Look for parasitized red blood cells.
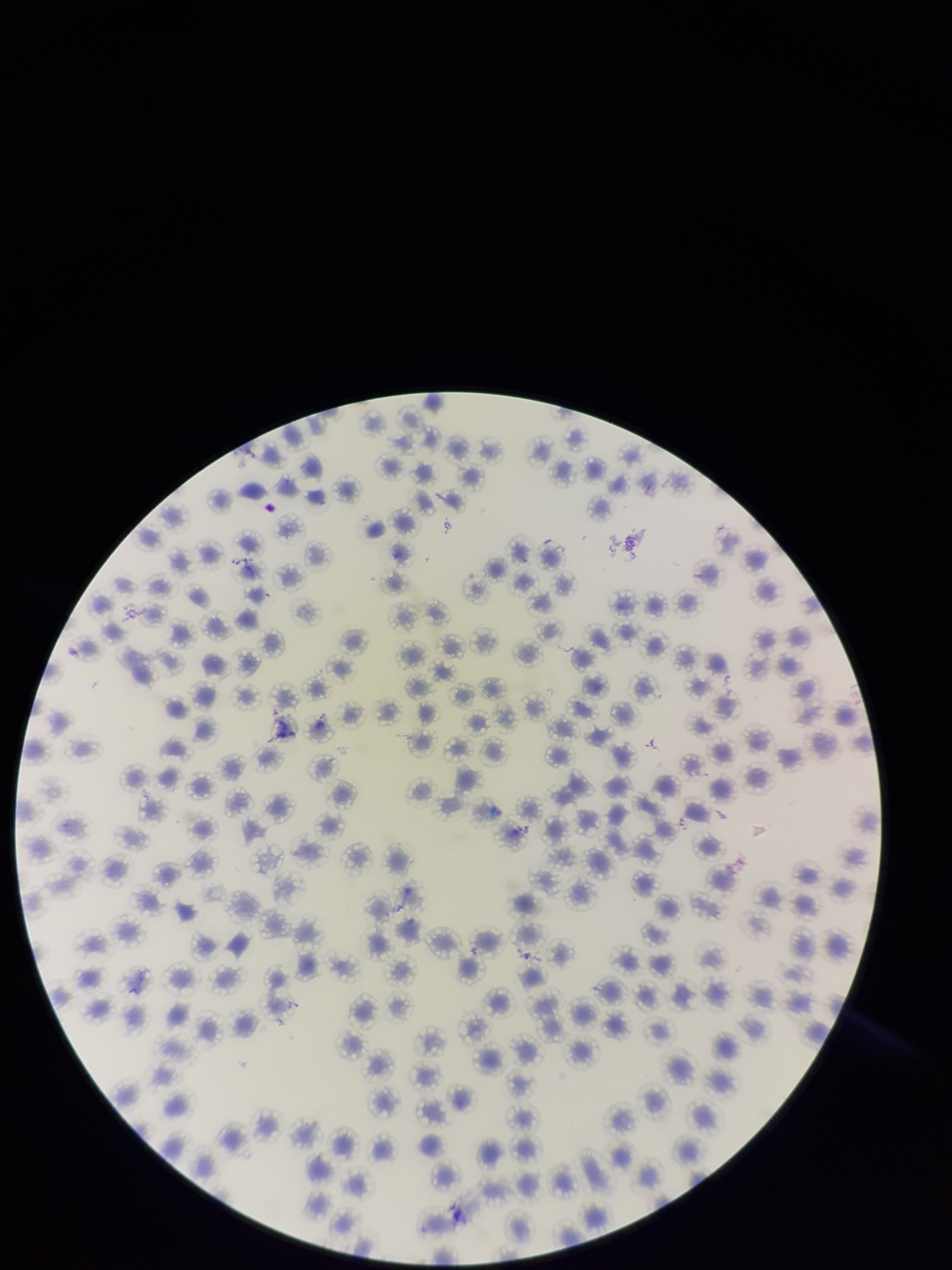
None seen.

Parasitized red blood cell count: 0. Image is 952×1270 pixels. Species reported for this patient: Plasmodium falciparum. Red blood cell count: 126. Smartphone photograph taken through the eyepiece of a microscope. Patient malaria status: infected. Single field of view. Stained with Giemsa. Preparation: thin smear.